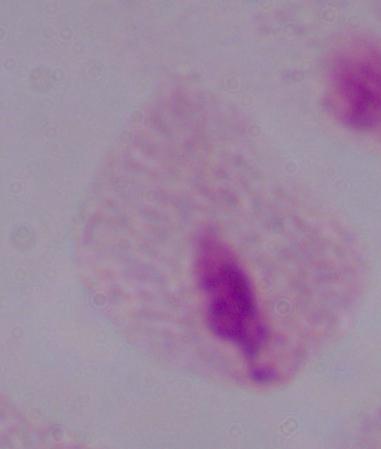

magnification = 1000x
identification = trichomonad
modality = photomicrograph